Assess the morphology of the red blood cells.
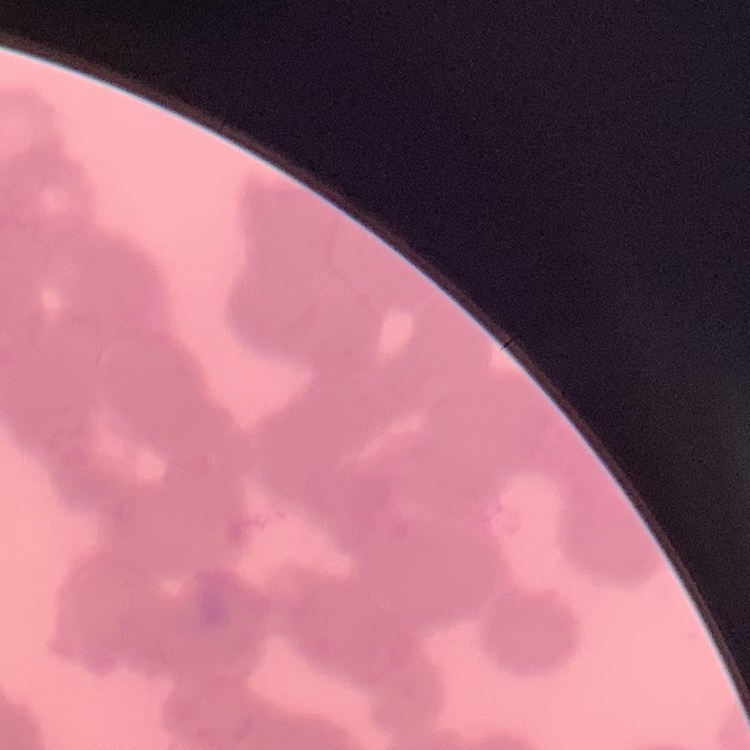
Rouleaux formation.

Summary:
  - Stain: Field's or Giemsa
  - Preparation: thin blood smear
  - Image type: one tile cut from a larger photomicrograph